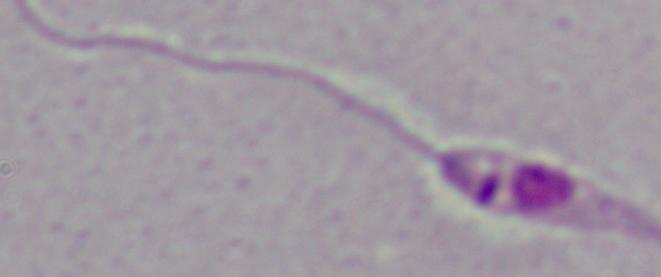
Summary:
  - Magnification: 1000x
  - Identification: Leishmania
  - Modality: micrograph